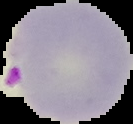

malaria status = parasitized
image size = 133×124 pixels
image type = segmented cell region with the area outside set to black
preparation = thin blood smear